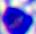
identification = leukocyte
modality = micrograph
magnification = 400x